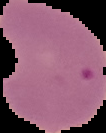
image type = segmented cell region on a black background
image size = 106×133 pixels
malaria status = parasitized
preparation = thin blood smear